State which parasite is depicted.
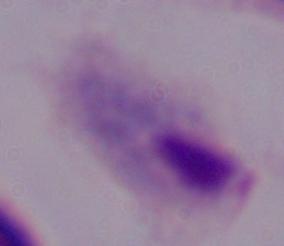
A trichomonad.

{
  "magnification": "1000x",
  "modality": "micrograph"
}